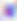

Summary:
  - Identification: Toxoplasma gondii
  - Magnification: 400x
  - Modality: photomicrograph